Identify the parasite.
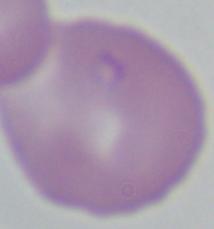

This is Babesia.

modality = micrograph
magnification = 1000x